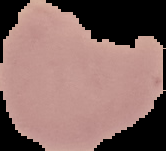
image size = 166×151 pixels
malaria status = uninfected
image type = cell region segmented out of the field of view; surrounding area masked to black
preparation = thin blood film